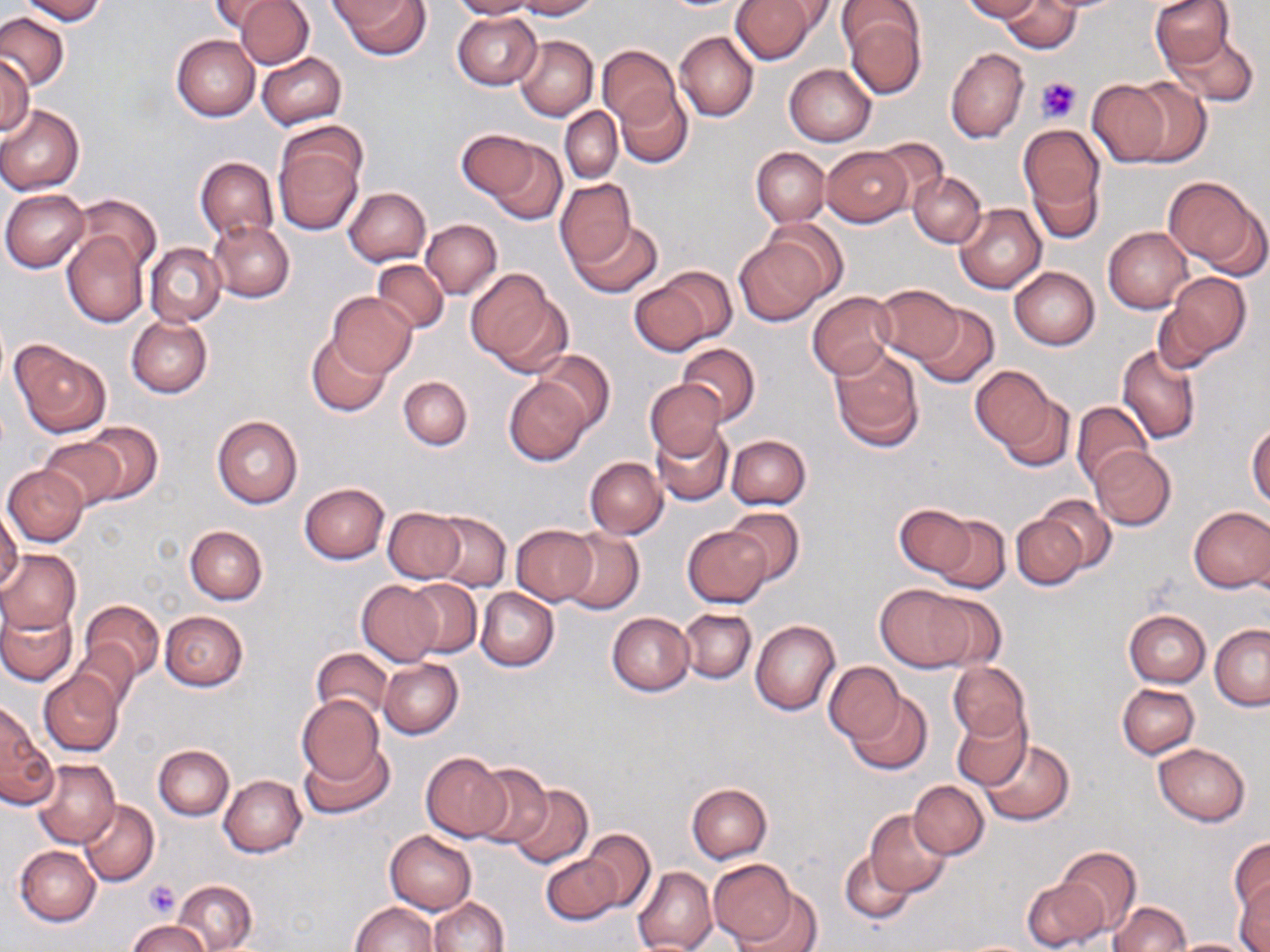 Approximate bounding boxes as named x1/y1/x2/y2 corners in pixels. Uninfected red blood cell locations: (x1=18, y1=0, x2=107, y2=24), (x1=208, y1=0, x2=281, y2=33), (x1=235, y1=0, x2=314, y2=69), (x1=333, y1=0, x2=430, y2=60), (x1=449, y1=0, x2=542, y2=19), (x1=517, y1=0, x2=600, y2=18), (x1=731, y1=0, x2=820, y2=64), (x1=963, y1=0, x2=1043, y2=22), (x1=1002, y1=0, x2=1078, y2=54), (x1=1150, y1=0, x2=1237, y2=72), (x1=839, y1=5, x2=926, y2=98), (x1=0, y1=12, x2=68, y2=89), (x1=452, y1=12, x2=540, y2=90), (x1=1165, y1=29, x2=1261, y2=107), (x1=675, y1=31, x2=759, y2=121), (x1=172, y1=34, x2=260, y2=121), (x1=514, y1=34, x2=598, y2=120), (x1=598, y1=45, x2=679, y2=128), (x1=946, y1=48, x2=1028, y2=142), (x1=257, y1=53, x2=346, y2=129), (x1=0, y1=57, x2=33, y2=137), (x1=784, y1=64, x2=876, y2=146), (x1=1125, y1=78, x2=1211, y2=166), (x1=1085, y1=80, x2=1174, y2=167), (x1=615, y1=86, x2=692, y2=166), (x1=0, y1=105, x2=84, y2=194), (x1=560, y1=108, x2=622, y2=183), (x1=1019, y1=125, x2=1105, y2=230), (x1=457, y1=130, x2=543, y2=201), (x1=275, y1=132, x2=364, y2=234), (x1=870, y1=139, x2=952, y2=209), (x1=489, y1=141, x2=566, y2=226), (x1=821, y1=146, x2=912, y2=226), (x1=751, y1=147, x2=828, y2=225), (x1=195, y1=157, x2=279, y2=241), (x1=909, y1=172, x2=985, y2=247), (x1=1162, y1=176, x2=1264, y2=273), (x1=554, y1=178, x2=638, y2=270), (x1=343, y1=187, x2=430, y2=266), (x1=1, y1=189, x2=90, y2=272), (x1=72, y1=194, x2=160, y2=276), (x1=954, y1=203, x2=1046, y2=294), (x1=422, y1=219, x2=502, y2=298), (x1=568, y1=220, x2=662, y2=298), (x1=759, y1=220, x2=849, y2=304), (x1=209, y1=221, x2=294, y2=302), (x1=1104, y1=226, x2=1193, y2=312), (x1=62, y1=234, x2=147, y2=326), (x1=734, y1=236, x2=831, y2=326), (x1=144, y1=242, x2=226, y2=326), (x1=372, y1=259, x2=448, y2=334), (x1=1008, y1=266, x2=1100, y2=349), (x1=465, y1=269, x2=563, y2=370), (x1=628, y1=273, x2=725, y2=355), (x1=1164, y1=273, x2=1252, y2=361), (x1=873, y1=283, x2=963, y2=364), (x1=329, y1=292, x2=418, y2=378), (x1=806, y1=292, x2=897, y2=379), (x1=912, y1=303, x2=999, y2=389), (x1=128, y1=316, x2=212, y2=397), (x1=307, y1=334, x2=389, y2=416), (x1=11, y1=341, x2=110, y2=436), (x1=676, y1=343, x2=760, y2=425), (x1=1116, y1=343, x2=1202, y2=444), (x1=829, y1=348, x2=925, y2=453), (x1=533, y1=349, x2=615, y2=432), (x1=970, y1=366, x2=1055, y2=451), (x1=398, y1=376, x2=472, y2=450), (x1=504, y1=378, x2=591, y2=464), (x1=644, y1=378, x2=725, y2=458), (x1=998, y1=394, x2=1074, y2=472), (x1=1072, y1=402, x2=1154, y2=489), (x1=212, y1=415, x2=302, y2=508), (x1=81, y1=422, x2=161, y2=503), (x1=1247, y1=423, x2=1270, y2=510), (x1=652, y1=424, x2=734, y2=506), (x1=726, y1=434, x2=810, y2=509), (x1=39, y1=435, x2=131, y2=510), (x1=1090, y1=446, x2=1175, y2=530), (x1=584, y1=456, x2=668, y2=539), (x1=4, y1=465, x2=88, y2=546), (x1=300, y1=482, x2=389, y2=563), (x1=1036, y1=495, x2=1116, y2=574), (x1=895, y1=503, x2=977, y2=577), (x1=1188, y1=505, x2=1270, y2=592), (x1=384, y1=507, x2=465, y2=582), (x1=723, y1=507, x2=804, y2=584), (x1=0, y1=509, x2=23, y2=595), (x1=430, y1=512, x2=511, y2=591), (x1=1011, y1=515, x2=1088, y2=589), (x1=932, y1=516, x2=1010, y2=595), (x1=185, y1=526, x2=267, y2=603), (x1=511, y1=526, x2=598, y2=605), (x1=683, y1=526, x2=770, y2=606), (x1=560, y1=527, x2=643, y2=614), (x1=0, y1=549, x2=81, y2=634), (x1=405, y1=579, x2=482, y2=657), (x1=358, y1=580, x2=443, y2=667), (x1=873, y1=584, x2=978, y2=672), (x1=476, y1=588, x2=558, y2=671), (x1=916, y1=592, x2=1008, y2=671), (x1=81, y1=599, x2=164, y2=682), (x1=1, y1=602, x2=76, y2=686), (x1=679, y1=608, x2=757, y2=683), (x1=1124, y1=609, x2=1211, y2=687), (x1=160, y1=610, x2=248, y2=691), (x1=607, y1=613, x2=694, y2=696), (x1=750, y1=619, x2=840, y2=715), (x1=1210, y1=625, x2=1270, y2=710), (x1=71, y1=639, x2=139, y2=711), (x1=311, y1=647, x2=392, y2=720), (x1=378, y1=658, x2=463, y2=738), (x1=825, y1=661, x2=903, y2=744), (x1=948, y1=661, x2=1030, y2=743), (x1=39, y1=670, x2=124, y2=756), (x1=1117, y1=684, x2=1199, y2=759), (x1=844, y1=692, x2=933, y2=776), (x1=296, y1=695, x2=384, y2=785), (x1=1, y1=703, x2=54, y2=806), (x1=952, y1=707, x2=1032, y2=790), (x1=978, y1=739, x2=1075, y2=826), (x1=301, y1=743, x2=393, y2=820), (x1=1153, y1=743, x2=1251, y2=825), (x1=154, y1=745, x2=234, y2=819), (x1=421, y1=752, x2=510, y2=843), (x1=33, y1=758, x2=119, y2=848), (x1=469, y1=764, x2=554, y2=850), (x1=219, y1=775, x2=307, y2=857), (x1=908, y1=780, x2=989, y2=859), (x1=508, y1=783, x2=593, y2=868), (x1=687, y1=783, x2=771, y2=863), (x1=79, y1=800, x2=159, y2=886), (x1=865, y1=810, x2=951, y2=896), (x1=578, y1=829, x2=656, y2=913), (x1=385, y1=830, x2=476, y2=913), (x1=1230, y1=835, x2=1269, y2=919), (x1=16, y1=845, x2=101, y2=926), (x1=1058, y1=846, x2=1142, y2=934), (x1=839, y1=849, x2=919, y2=926), (x1=542, y1=851, x2=622, y2=924), (x1=708, y1=859, x2=797, y2=944), (x1=632, y1=866, x2=717, y2=952), (x1=1233, y1=875, x2=1270, y2=951), (x1=1021, y1=876, x2=1111, y2=952), (x1=174, y1=880, x2=257, y2=951), (x1=730, y1=888, x2=823, y2=952), (x1=428, y1=898, x2=509, y2=952), (x1=1109, y1=901, x2=1189, y2=952), (x1=350, y1=902, x2=438, y2=952), (x1=127, y1=920, x2=212, y2=952), (x1=1165, y1=937, x2=1260, y2=951). Platelet locations: (x1=1036, y1=76, x2=1081, y2=124), (x1=143, y1=879, x2=180, y2=917). Slide-level diagnosis: no evidence of blood parasites. May-Grünwald-Giemsa-stained preparation. Single field of view. Thin blood film. Image is 1270×952 pixels. Captured at 1000x magnification. Optical microscopy.